Outline every leukocyte.
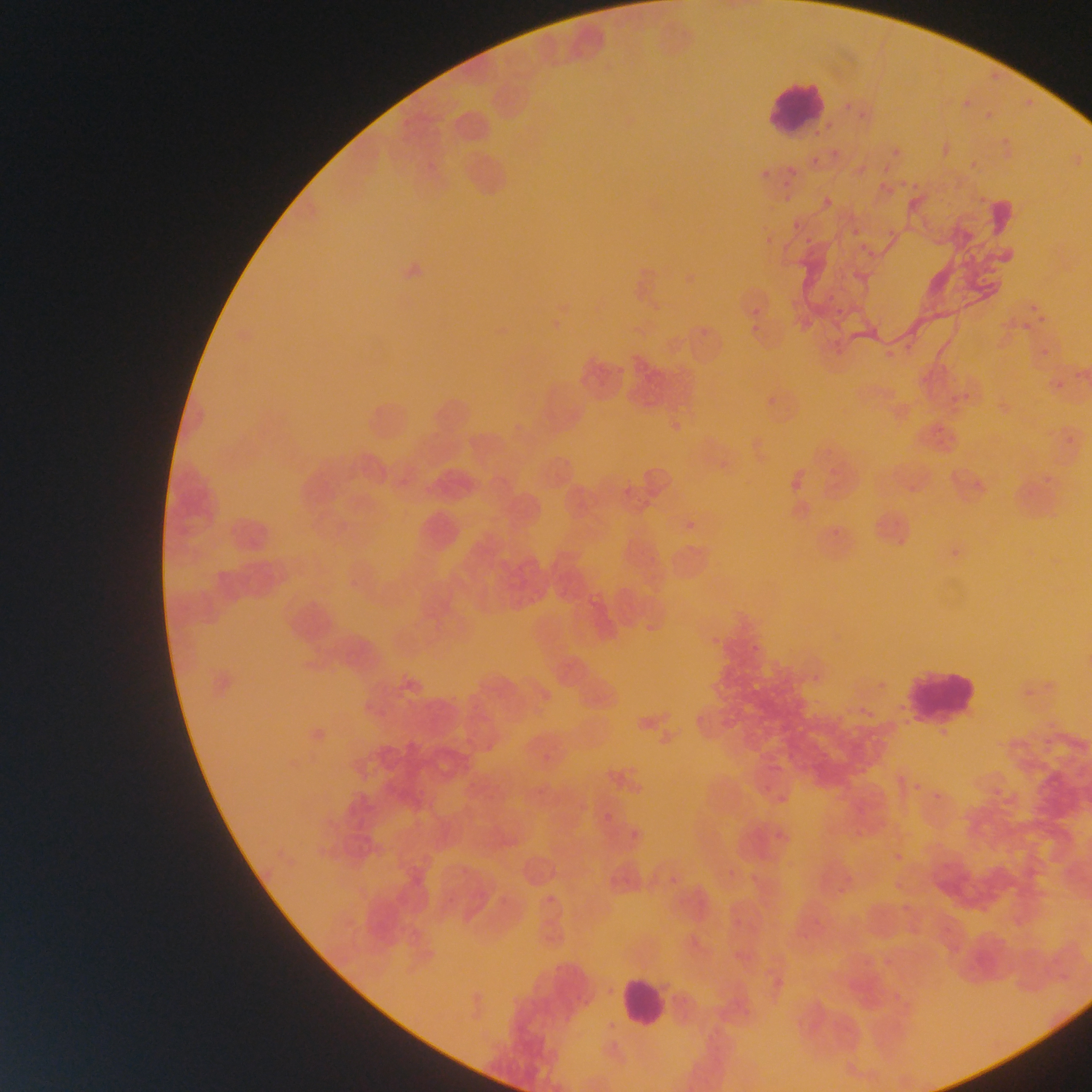
Approximate bounding boxes as {left, top, right, bottom} in pixels.
Leukocytes: {761, 77, 832, 139}, {903, 673, 977, 721}, {617, 972, 669, 1032}.

Summary:
  - Plasmodium parasite locations: {986, 69, 1002, 82}, {963, 92, 976, 113}, {1022, 93, 1041, 105}, {859, 112, 867, 119}, {996, 136, 1012, 150}, {938, 137, 959, 161}, {887, 142, 903, 157}, {810, 150, 824, 172}, {771, 161, 803, 205}, {910, 173, 934, 192}, {885, 178, 904, 198}, {815, 191, 835, 215}, {976, 192, 989, 212}, {846, 224, 868, 239}, {856, 251, 877, 259}, {745, 300, 772, 320}, {1021, 305, 1044, 331}, {667, 422, 680, 437}, {787, 468, 803, 491}, {679, 512, 700, 538}, {826, 523, 841, 536}, {944, 547, 964, 561}, {707, 632, 720, 650}, {748, 640, 766, 654}, {874, 673, 888, 694}, {1017, 681, 1040, 700}, {856, 701, 879, 723}, {544, 754, 551, 762}, {895, 767, 907, 786}, {925, 783, 944, 814}, {775, 792, 794, 815}, {605, 813, 614, 822}, {853, 825, 864, 844}, {888, 849, 904, 868}, {548, 895, 556, 903}
  - Preparation: thin blood film
  - Field of view: single
  - Image size: 1092×1092 pixels
  - Country: Ghana
  - Capture: mobile-phone photograph through a microscope